State which parasite is depicted.
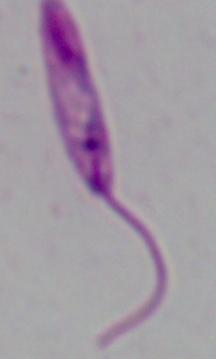

Leishmania.

Summary:
  - Magnification: 1000x
  - Modality: micrograph